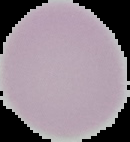
Summary:
  - Image size: 130×142 pixels
  - Image type: segmented cell region on a black background
  - Preparation: thin blood smear
  - Result: negative for Plasmodium parasites